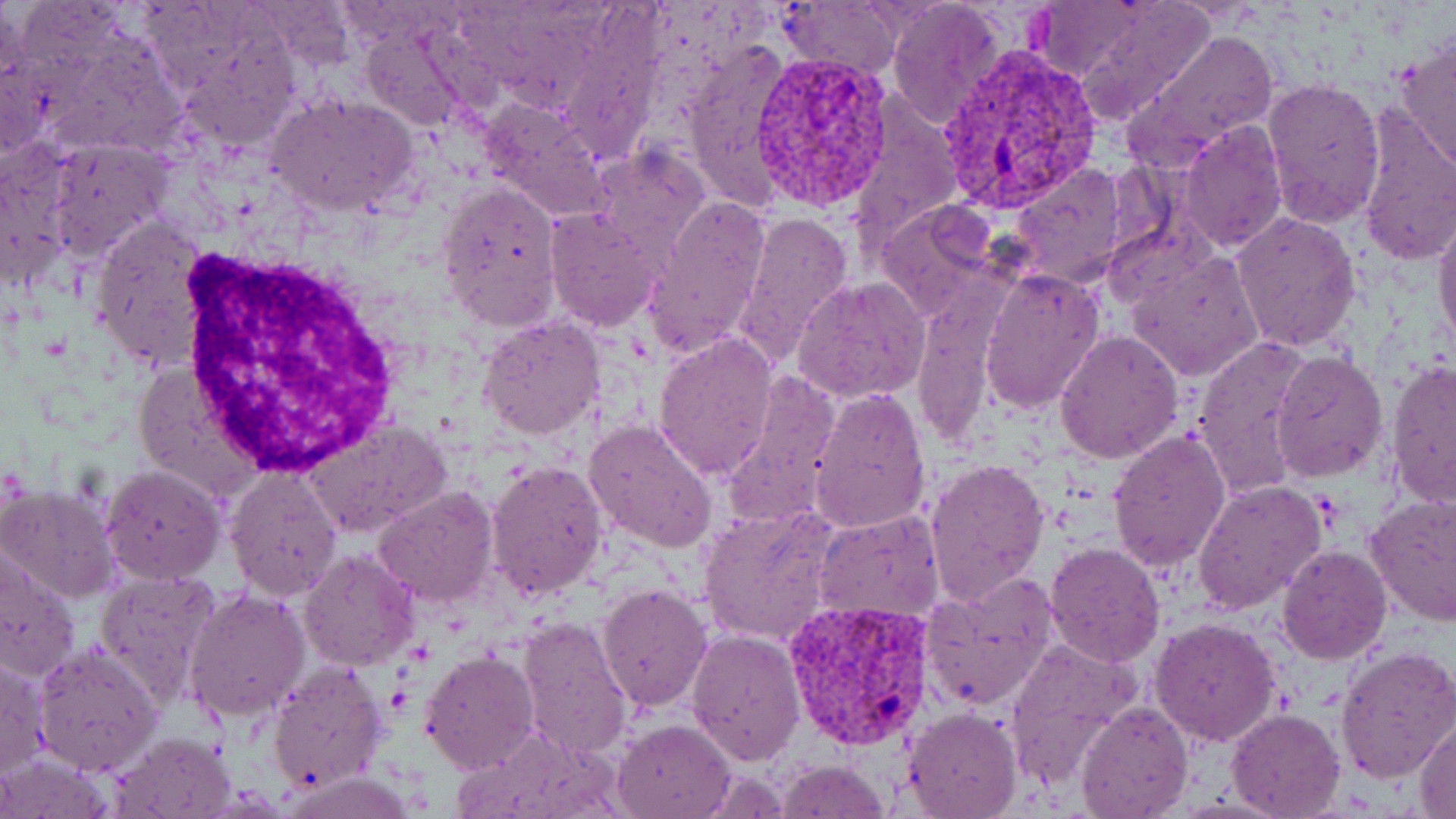

Summary:
  - Coordinate format: approximate bounding boxes as named x1/y1/x2/y2 corners in pixels
  - Plasmodium vivax-infected red blood cell locations: (x1=938, y1=46, x2=1106, y2=211), (x1=746, y1=52, x2=895, y2=214), (x1=782, y1=598, x2=937, y2=750)
  - White blood cell locations: (x1=166, y1=252, x2=403, y2=473)
  - Uninfected red blood cell locations: (x1=885, y1=0, x2=1007, y2=129), (x1=1054, y1=0, x2=1216, y2=129), (x1=777, y1=1, x2=902, y2=82), (x1=1033, y1=2, x2=1146, y2=85), (x1=359, y1=27, x2=472, y2=132), (x1=1126, y1=27, x2=1280, y2=167), (x1=1394, y1=35, x2=1456, y2=175), (x1=682, y1=43, x2=791, y2=211), (x1=1, y1=52, x2=47, y2=164), (x1=1260, y1=79, x2=1385, y2=229), (x1=267, y1=93, x2=420, y2=218), (x1=482, y1=98, x2=611, y2=225), (x1=846, y1=107, x2=959, y2=246), (x1=1352, y1=107, x2=1456, y2=267), (x1=1177, y1=120, x2=1288, y2=253), (x1=45, y1=140, x2=172, y2=261), (x1=0, y1=143, x2=77, y2=291), (x1=586, y1=146, x2=711, y2=263), (x1=1007, y1=163, x2=1128, y2=289), (x1=436, y1=179, x2=562, y2=331), (x1=644, y1=195, x2=773, y2=361), (x1=873, y1=201, x2=997, y2=321), (x1=1432, y1=202, x2=1456, y2=355), (x1=544, y1=209, x2=666, y2=331), (x1=731, y1=210, x2=855, y2=368), (x1=1230, y1=212, x2=1361, y2=353), (x1=91, y1=213, x2=216, y2=373), (x1=1104, y1=214, x2=1214, y2=309), (x1=1127, y1=252, x2=1265, y2=381), (x1=979, y1=267, x2=1106, y2=415), (x1=793, y1=277, x2=930, y2=402), (x1=913, y1=292, x2=998, y2=451), (x1=478, y1=314, x2=606, y2=441), (x1=1056, y1=331, x2=1184, y2=463), (x1=653, y1=332, x2=778, y2=481), (x1=1190, y1=340, x2=1312, y2=493), (x1=1271, y1=350, x2=1389, y2=484), (x1=1385, y1=362, x2=1455, y2=509), (x1=726, y1=371, x2=842, y2=522), (x1=808, y1=387, x2=931, y2=533), (x1=303, y1=417, x2=454, y2=540), (x1=584, y1=418, x2=717, y2=556), (x1=1108, y1=430, x2=1232, y2=572), (x1=925, y1=457, x2=1050, y2=606), (x1=485, y1=458, x2=608, y2=602), (x1=101, y1=464, x2=227, y2=586), (x1=224, y1=467, x2=342, y2=601), (x1=1194, y1=479, x2=1325, y2=615), (x1=0, y1=484, x2=119, y2=603), (x1=372, y1=485, x2=500, y2=609), (x1=1365, y1=497, x2=1456, y2=625), (x1=699, y1=506, x2=839, y2=643), (x1=814, y1=509, x2=946, y2=627), (x1=1044, y1=541, x2=1165, y2=666), (x1=1276, y1=544, x2=1391, y2=665), (x1=298, y1=547, x2=419, y2=672), (x1=0, y1=550, x2=81, y2=683), (x1=94, y1=569, x2=224, y2=705), (x1=922, y1=576, x2=1058, y2=713), (x1=595, y1=584, x2=713, y2=712), (x1=184, y1=587, x2=311, y2=723), (x1=1150, y1=616, x2=1280, y2=746), (x1=516, y1=617, x2=632, y2=759), (x1=686, y1=630, x2=806, y2=765), (x1=1005, y1=637, x2=1140, y2=784), (x1=34, y1=643, x2=161, y2=776), (x1=1334, y1=645, x2=1456, y2=781), (x1=419, y1=647, x2=540, y2=774), (x1=1, y1=655, x2=49, y2=779), (x1=268, y1=659, x2=388, y2=795), (x1=1079, y1=700, x2=1191, y2=819), (x1=1226, y1=707, x2=1344, y2=817), (x1=902, y1=708, x2=1021, y2=819), (x1=1411, y1=715, x2=1456, y2=815), (x1=614, y1=718, x2=736, y2=818), (x1=112, y1=732, x2=236, y2=819), (x1=0, y1=753, x2=113, y2=818), (x1=775, y1=758, x2=892, y2=818), (x1=695, y1=765, x2=790, y2=817), (x1=283, y1=772, x2=416, y2=818)
  - Slide-level diagnosis: Plasmodium vivax
  - Magnification: 1000x
  - Modality: optical microscopy
  - Preparation: thin blood smear
  - Stain: May-Grünwald-Giemsa
  - Image size: 1456×819 pixels
  - Field of view: single